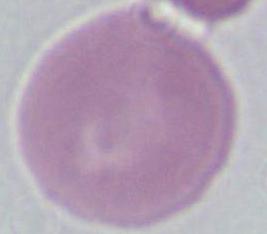 Micrograph. An erythrocyte is shown. Captured at 1000x magnification.